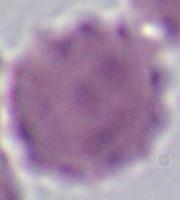
{
  "identification": "erythrocyte",
  "modality": "photomicrograph",
  "magnification": "1000x"
}